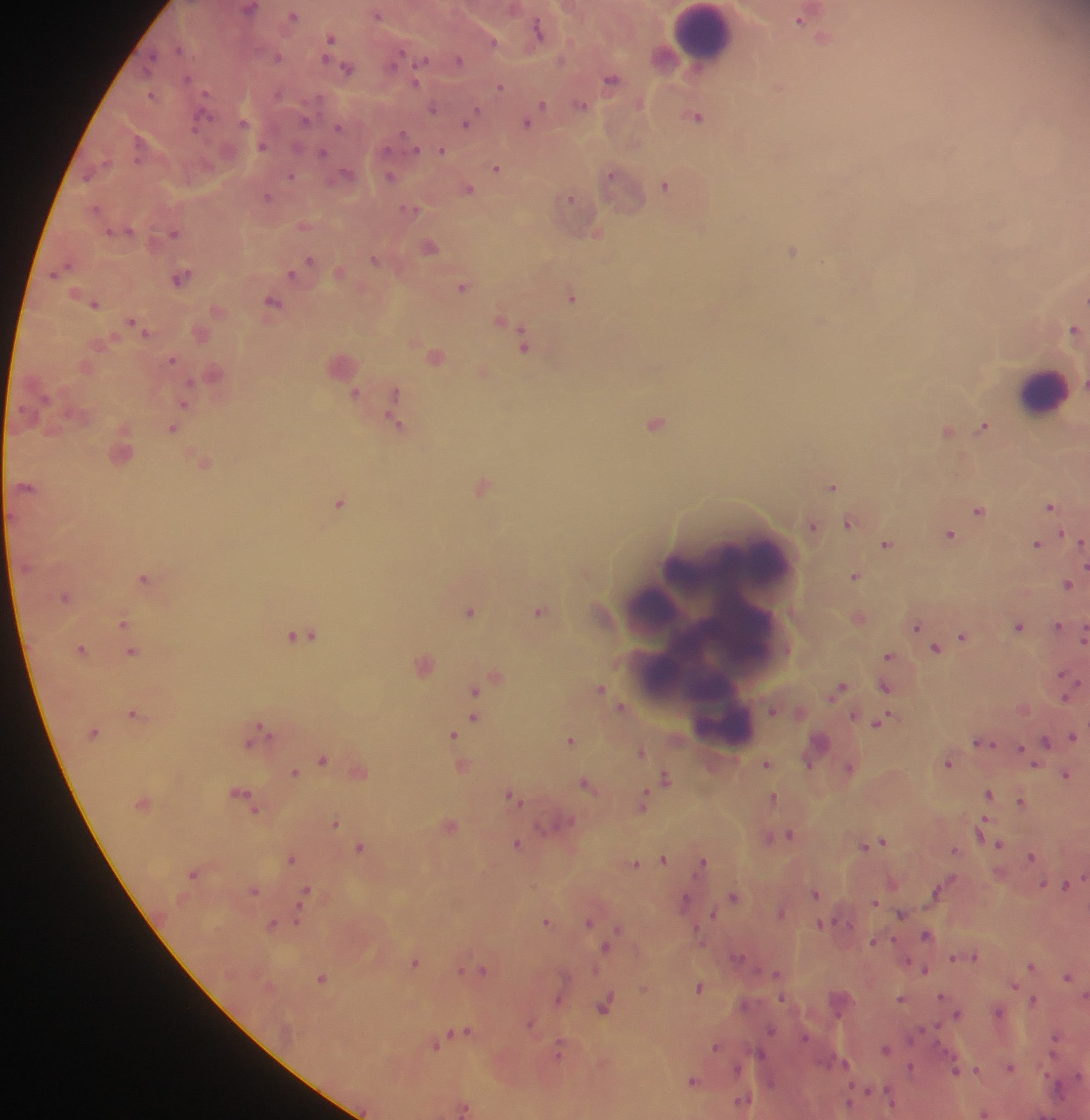
Approximate centers as [x, y] in pixels.
Summary:
  - Plasmodium parasite locations: [249, 9], [376, 15], [292, 16], [799, 20], [538, 29], [329, 39], [492, 42], [177, 49], [277, 57], [150, 59], [324, 59], [423, 59], [395, 60], [458, 60], [560, 61], [347, 69], [188, 78], [611, 79], [415, 83], [500, 87], [278, 94], [149, 95], [542, 104], [580, 105], [432, 108], [696, 117], [200, 119], [304, 120], [242, 122], [466, 123], [526, 123], [338, 128], [402, 133], [261, 147], [415, 150], [441, 151], [322, 152], [496, 167], [346, 173], [610, 174], [290, 176], [85, 177], [389, 178], [664, 186], [467, 188], [265, 197], [568, 197], [95, 208], [410, 209], [109, 233], [173, 233], [596, 234], [429, 248], [792, 251], [373, 259], [308, 261], [290, 274], [180, 277], [461, 287], [571, 298], [272, 302], [93, 305], [131, 321], [1073, 328], [522, 344], [171, 359], [189, 382], [354, 393], [394, 393], [184, 405], [655, 422], [395, 423], [983, 426], [172, 430], [946, 431], [26, 486], [481, 486], [831, 486], [339, 502], [1049, 506], [977, 510], [848, 522], [811, 527], [949, 534], [1060, 534], [1036, 543], [886, 544], [1085, 566], [854, 576], [143, 578], [1067, 584], [64, 597], [468, 612], [539, 612], [122, 622], [916, 626], [1057, 626], [1018, 627], [299, 635], [1083, 635], [961, 637], [80, 649], [935, 649], [130, 652], [886, 656], [1061, 674], [884, 687], [600, 689], [839, 689], [474, 691], [1064, 698], [621, 707], [773, 710], [132, 714], [473, 719], [880, 721], [260, 728], [452, 735], [1072, 736], [251, 741], [570, 741], [1045, 742], [983, 743], [1019, 749], [641, 751], [321, 759], [807, 763], [947, 763], [765, 764], [848, 767], [293, 773], [1065, 775], [665, 777], [586, 785], [988, 794], [241, 796], [510, 796], [773, 797], [1020, 801], [643, 802], [251, 807], [334, 822], [982, 824], [789, 834], [767, 838], [881, 842], [516, 844], [999, 844], [865, 846], [359, 848], [954, 851], [1030, 856], [291, 859], [662, 859], [702, 862], [634, 864], [193, 874], [1042, 884], [1066, 886], [252, 891], [935, 891], [304, 892], [815, 894], [733, 896], [683, 901], [873, 902], [781, 912], [299, 914], [712, 914], [901, 914], [545, 921], [588, 922], [270, 924], [820, 924], [615, 931], [925, 934], [873, 942], [607, 945], [973, 956], [737, 957], [952, 958], [413, 963], [1030, 966], [459, 970], [481, 970], [924, 970], [594, 971], [776, 973], [1067, 977], [321, 978], [1013, 986], [698, 987], [941, 996], [557, 999], [782, 999], [900, 999], [1034, 999], [744, 1004], [603, 1006], [999, 1012], [957, 1014], [529, 1024], [770, 1029], [465, 1030], [804, 1037], [911, 1037], [1055, 1037], [436, 1045], [715, 1046], [885, 1048], [558, 1050], [760, 1053], [844, 1063], [910, 1067], [1009, 1067], [736, 1069], [955, 1070], [976, 1070], [691, 1081], [770, 1083], [742, 1100], [848, 1102], [463, 1109], [984, 1114]
  - Leukocyte locations: [703, 31], [1042, 391], [713, 637]
  - Country: Ghana
  - Field of view: single
  - Preparation: thick blood smear
  - Capture: mobile-phone photograph through a microscope
  - Image size: 1090×1120 pixels